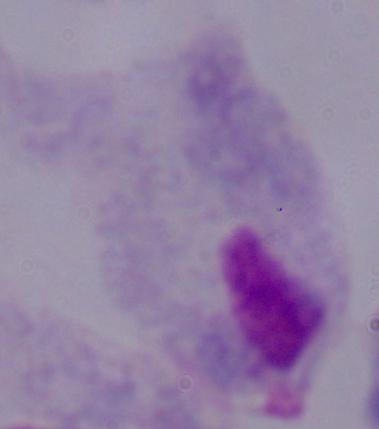
Summary:
  - Modality: photomicrograph
  - Magnification: 1000x
  - Identification: trichomonad